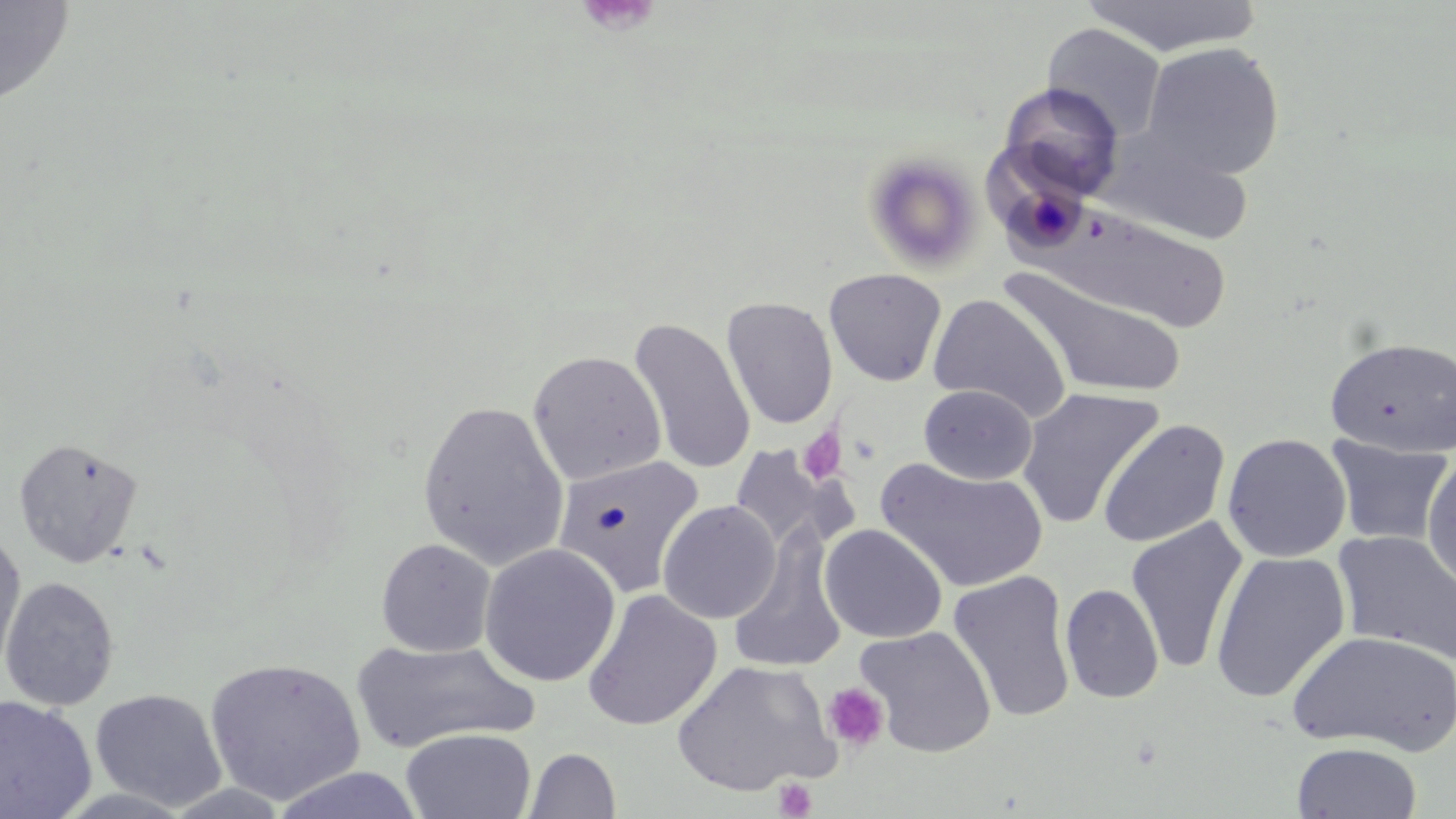
Summary:
  - Coordinate format: approximate bounding boxes as named x1/y1/x2/y2 corners in pixels
  - Platelet locations (subset): (x1=797, y1=427, x2=847, y2=485), (x1=821, y1=682, x2=891, y2=754), (x1=773, y1=778, x2=818, y2=819)
  - Uninfected red blood cell locations (subset): (x1=0, y1=0, x2=76, y2=109), (x1=1080, y1=0, x2=1262, y2=57), (x1=1042, y1=23, x2=1167, y2=141), (x1=1141, y1=42, x2=1285, y2=181), (x1=999, y1=83, x2=1123, y2=200), (x1=1096, y1=127, x2=1254, y2=246), (x1=862, y1=152, x2=984, y2=276), (x1=1031, y1=206, x2=1230, y2=332), (x1=1000, y1=265, x2=1189, y2=398), (x1=823, y1=268, x2=947, y2=386), (x1=928, y1=293, x2=1071, y2=422), (x1=722, y1=297, x2=838, y2=429), (x1=629, y1=318, x2=756, y2=475), (x1=1325, y1=336, x2=1456, y2=457), (x1=527, y1=350, x2=666, y2=485), (x1=919, y1=384, x2=1037, y2=484), (x1=1017, y1=387, x2=1164, y2=529), (x1=417, y1=399, x2=568, y2=570), (x1=1098, y1=419, x2=1231, y2=549), (x1=1222, y1=433, x2=1351, y2=562), (x1=1326, y1=435, x2=1452, y2=547), (x1=13, y1=437, x2=143, y2=569), (x1=728, y1=443, x2=855, y2=558), (x1=1422, y1=454, x2=1456, y2=593), (x1=554, y1=455, x2=707, y2=599), (x1=877, y1=458, x2=1048, y2=593), (x1=657, y1=500, x2=781, y2=624), (x1=1125, y1=517, x2=1249, y2=675), (x1=820, y1=524, x2=947, y2=644), (x1=728, y1=529, x2=848, y2=675), (x1=1334, y1=530, x2=1456, y2=665), (x1=0, y1=536, x2=26, y2=680), (x1=376, y1=538, x2=496, y2=657), (x1=479, y1=543, x2=620, y2=687), (x1=1210, y1=550, x2=1351, y2=704), (x1=948, y1=571, x2=1076, y2=723), (x1=1, y1=576, x2=119, y2=711), (x1=1060, y1=583, x2=1164, y2=704), (x1=582, y1=590, x2=722, y2=731), (x1=1288, y1=629, x2=1456, y2=756), (x1=350, y1=638, x2=540, y2=754), (x1=204, y1=657, x2=367, y2=806), (x1=671, y1=660, x2=840, y2=797), (x1=90, y1=688, x2=227, y2=811), (x1=0, y1=696, x2=97, y2=818), (x1=401, y1=728, x2=537, y2=819), (x1=1292, y1=741, x2=1421, y2=819), (x1=524, y1=747, x2=622, y2=819), (x1=267, y1=766, x2=428, y2=819)
  - Slide-level diagnosis: negative for blood parasites
  - Field of view: single
  - Modality: light microscopy
  - Stain: May-Grünwald-Giemsa
  - Image size: 1456×819 pixels
  - Preparation: thin blood smear
  - Magnification: 1000x